Locate every Plasmodium falciparum-infected red blood cell.
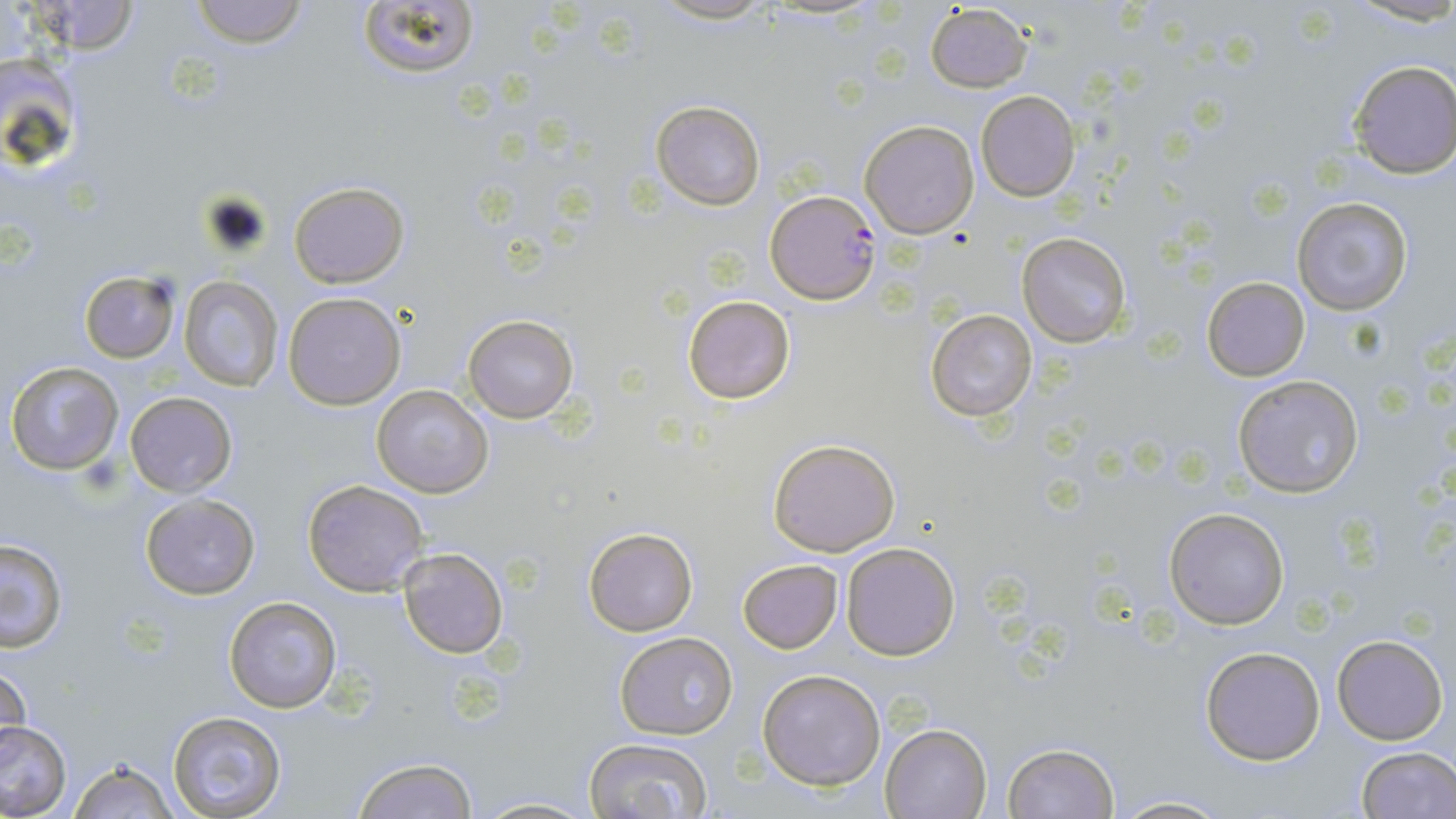
Approximate bounding boxes as (x1,y1)-(x2,y2) corner pairs in pixels.
Plasmodium falciparum-infected red blood cells: (767,191)-(881,303).

Uninfected red blood cell locations: (25,0)-(143,56), (188,0)-(310,47), (356,0)-(480,83), (645,0)-(785,25), (926,4)-(1033,93), (1346,59)-(1456,178), (976,91)-(1080,201), (651,100)-(765,209), (859,119)-(979,238), (289,180)-(409,288), (1291,196)-(1413,316), (1019,233)-(1132,347), (80,270)-(180,362), (179,276)-(283,393), (1202,276)-(1311,382), (282,291)-(406,410), (683,294)-(794,404), (926,309)-(1037,423), (463,314)-(578,422), (6,360)-(123,476), (1233,375)-(1364,497), (371,384)-(493,498), (124,391)-(239,497), (768,437)-(901,557), (301,479)-(427,596), (141,494)-(260,600), (1164,506)-(1291,630), (584,527)-(698,637), (0,539)-(68,652), (842,543)-(959,660), (398,547)-(509,659), (736,559)-(843,654), (224,596)-(343,713), (613,632)-(739,739), (1332,633)-(1448,745), (1199,644)-(1328,766), (1,658)-(31,762), (757,669)-(887,790), (166,710)-(285,817), (0,719)-(73,819), (880,722)-(992,818), (582,737)-(713,819), (1001,742)-(1121,818), (1353,745)-(1455,819), (351,757)-(476,819), (68,758)-(178,818), (1108,794)-(1233,818), (474,796)-(597,818). Slide-level diagnosis: Plasmodium falciparum. May-Grünwald-Giemsa stain. Thin blood smear. Image is 1456×819 pixels. 1000x magnification. Light microscopy. One field of a larger specimen.